Assess this cell for malaria.
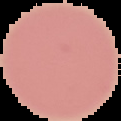
Uninfected.

Summary:
  - Preparation: thin blood smear
  - Image size: 121×121 pixels
  - Image type: segmented cell region with the area outside set to black